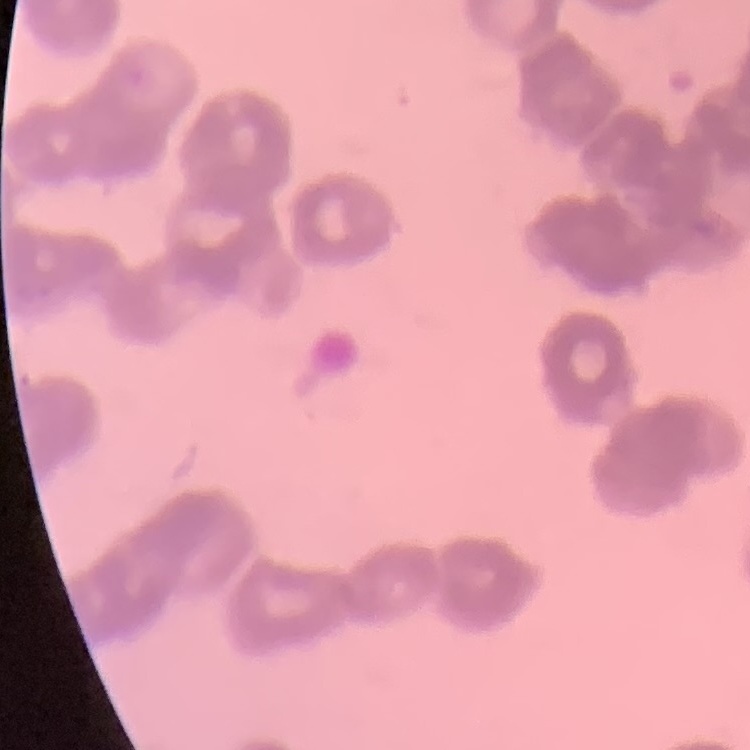

Summary:
  - Red blood cell morphology: rouleaux formation
  - Stain: Field's or Giemsa
  - Preparation: thin blood smear
  - Image type: square crop of a larger photomicrograph